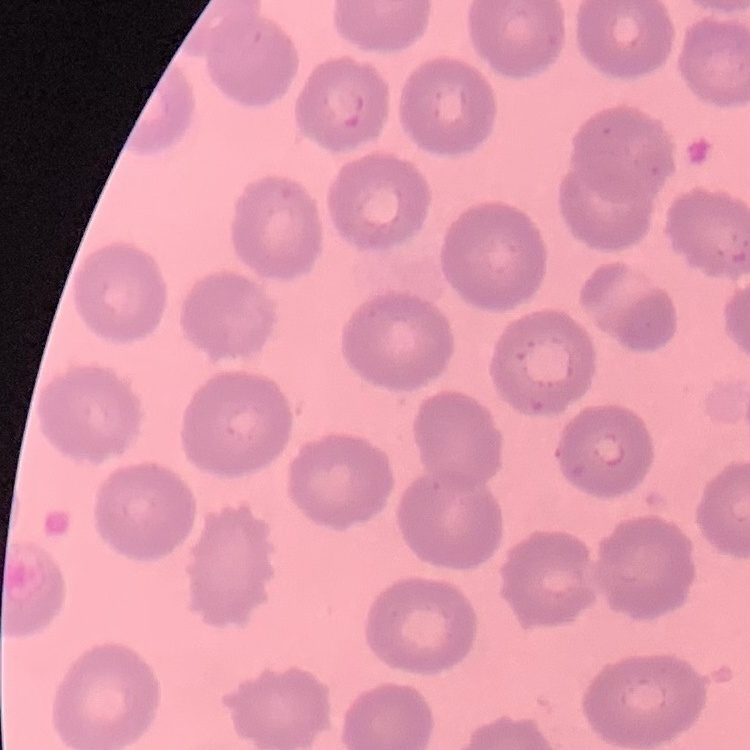 The red blood cells exhibit no rouleaux formation. Stained with either Field's or Giemsa. Square crop of a larger photomicrograph. Thin blood film.